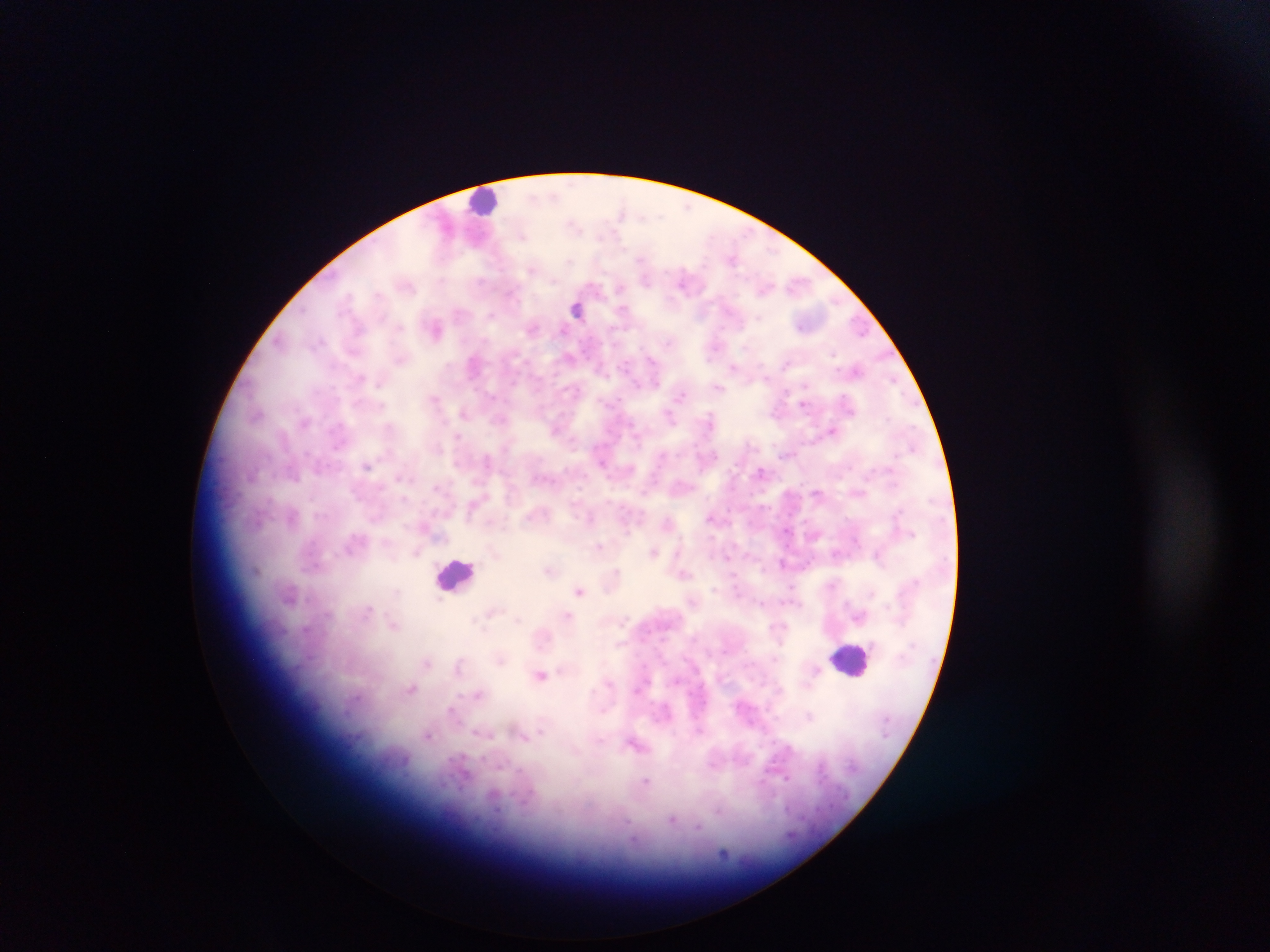
Approximate centers as (x, y) in pixels.
Summary:
  - Plasmodium parasite locations: (554, 195), (619, 213), (573, 225), (523, 236), (732, 258), (641, 259), (569, 260), (531, 270), (645, 280), (682, 281), (407, 286), (619, 289), (765, 289), (378, 295), (512, 295), (576, 309), (623, 311), (702, 313), (492, 315), (860, 326), (399, 327), (532, 328), (437, 329), (560, 329), (279, 341), (745, 346), (833, 354), (569, 357), (401, 359), (652, 360), (473, 364), (786, 364), (732, 367), (857, 370), (765, 378), (360, 379), (894, 381), (655, 382), (380, 383), (806, 386), (718, 388), (573, 391), (680, 396), (435, 399), (803, 403), (381, 406), (464, 412), (257, 415), (670, 417), (709, 419), (305, 422), (832, 430), (636, 435), (458, 436), (912, 448), (784, 453), (714, 456), (486, 459), (602, 463), (367, 465), (761, 472), (293, 476), (399, 477), (437, 487), (817, 493), (404, 499), (293, 516), (590, 518), (710, 518), (668, 521), (786, 530), (599, 546), (349, 549), (416, 552), (653, 552), (835, 554), (877, 554), (727, 557), (782, 563), (549, 570), (256, 571), (617, 571), (684, 574), (736, 589), (579, 591), (872, 593), (438, 600), (760, 603), (368, 609), (491, 613), (568, 616), (860, 616), (517, 619), (624, 620), (393, 624), (500, 660), (427, 662), (460, 665), (816, 670), (540, 675), (410, 688), (478, 694), (451, 712), (809, 715), (541, 732), (428, 735), (524, 735), (635, 744), (786, 778), (646, 781), (672, 820), (698, 828), (724, 854)
  - Leukocyte locations: (486, 202), (456, 575), (851, 660)
  - Field of view: single
  - Image size: 1270×952 pixels
  - Capture: mobile-phone photograph through a microscope
  - Preparation: thick blood smear
  - Country: Ghana